Assess this cell for malaria.
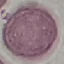
It is uninfected.

image type = automatically extracted cell patch, resized to 64 × 64 pixels
stain = Giemsa
capture = smartphone through the microscope eyepiece
preparation = thin smear